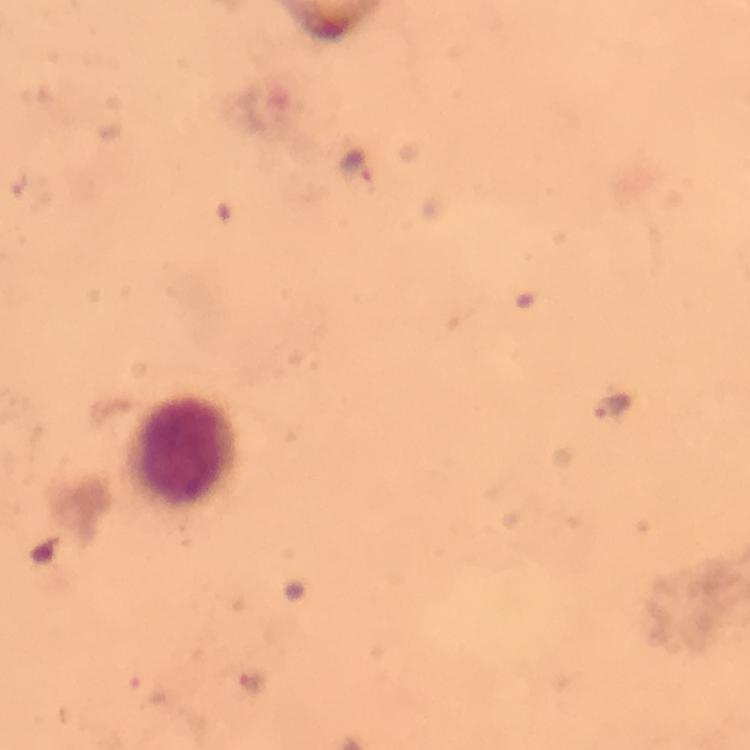
Approximate object centers, in pixels from the top-left corner. Malaria parasite locations: (x=355, y=167), (x=616, y=405), (x=250, y=681). Leukocyte locations: (x=185, y=448). A crop from one field of view. Giemsa stain. From a diagnostic examination for malaria. Thick blood smear. Immersion oil was used. Photographed through the microscope with a smartphone camera. 100x magnification. Image is 750×750 pixels.